State which cell type is depicted.
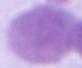

An erythrocyte.

Captured at 1000x magnification. Micrograph.